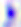 Toxoplasma gondii is seen. Micrograph. Captured at 400x magnification.